Name the blood parasite species.
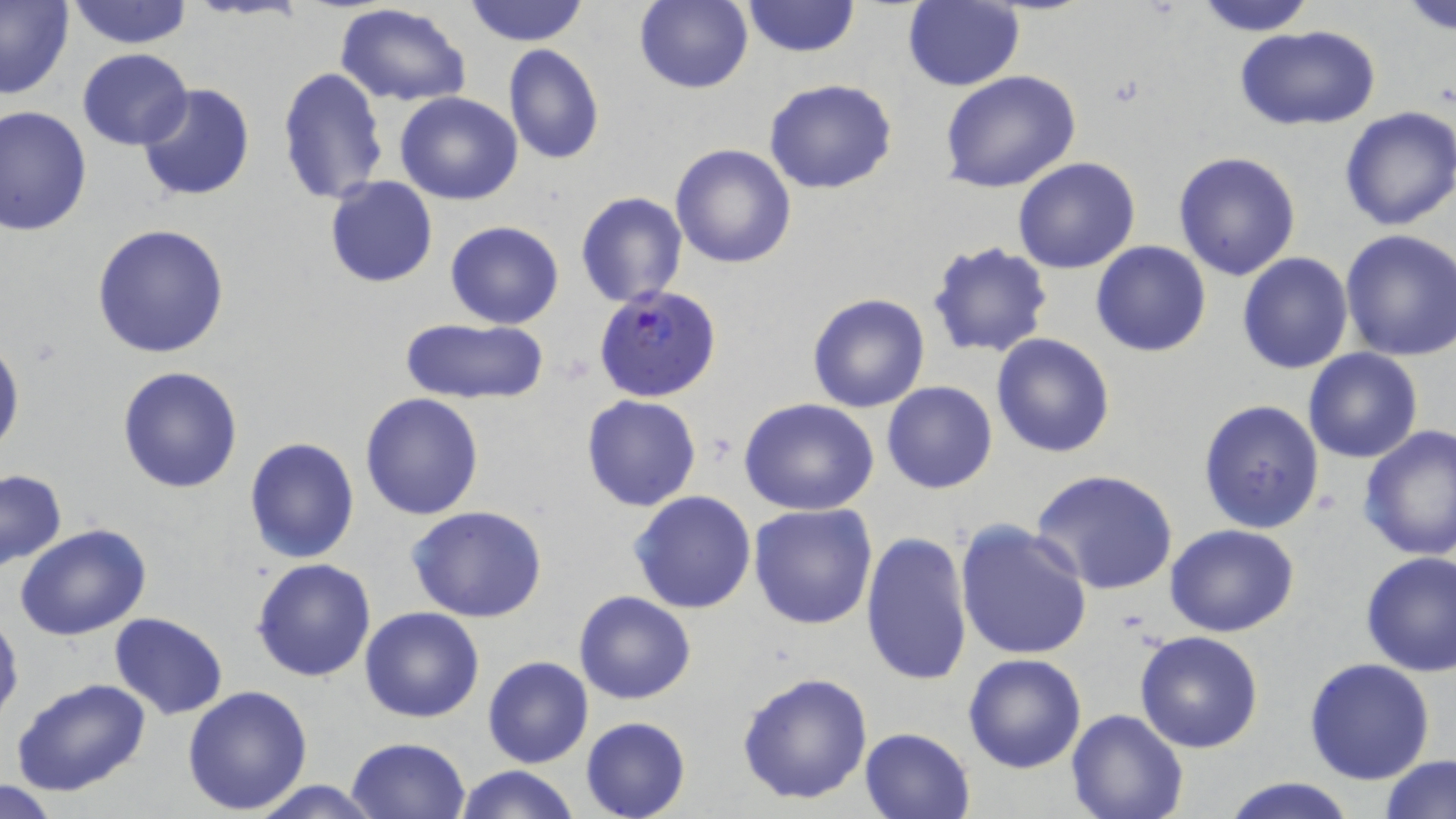

Plasmodium falciparum.

Summary:
  - Coordinate format: approximate bounding boxes as (x1, y1, x2, y2) in pixels
  - Uninfected red blood cell locations: (0, 0, 78, 101), (463, 0, 590, 46), (631, 0, 754, 95), (1190, 0, 1319, 35), (65, 1, 194, 50), (741, 1, 860, 58), (1397, 1, 1456, 35), (901, 2, 1025, 90), (334, 4, 474, 107), (1234, 25, 1382, 130), (502, 45, 604, 165), (77, 49, 192, 150), (277, 66, 390, 207), (937, 69, 1081, 194), (763, 79, 898, 195), (135, 83, 254, 202), (396, 91, 523, 205), (0, 103, 94, 236), (1338, 105, 1456, 232), (670, 144, 797, 268), (1172, 151, 1302, 282), (1013, 157, 1141, 274), (324, 175, 438, 288), (575, 192, 688, 307), (445, 221, 564, 329), (92, 223, 230, 360), (1338, 229, 1456, 361), (926, 240, 1055, 358), (1090, 240, 1212, 358), (1236, 252, 1355, 374), (806, 292, 931, 413), (398, 316, 549, 405), (990, 332, 1116, 458), (0, 334, 24, 461), (1302, 348, 1423, 462), (115, 365, 243, 494), (881, 380, 997, 494), (360, 392, 486, 520), (580, 393, 703, 511), (739, 399, 880, 515), (1198, 399, 1326, 536), (1357, 424, 1456, 564), (244, 436, 360, 565), (1030, 468, 1178, 595), (1, 470, 67, 571), (628, 489, 758, 613), (748, 503, 879, 630), (407, 505, 550, 623), (952, 520, 1094, 662), (1164, 524, 1299, 637), (14, 526, 151, 642), (860, 529, 974, 687), (1358, 552, 1456, 678), (251, 556, 378, 682), (574, 590, 696, 706), (0, 606, 23, 730), (359, 606, 485, 723), (109, 612, 228, 719), (1133, 631, 1264, 754), (963, 653, 1087, 774), (482, 655, 593, 768), (1303, 658, 1435, 785), (736, 671, 873, 806), (11, 678, 154, 799), (181, 685, 314, 814), (1064, 710, 1188, 819), (580, 717, 691, 819), (858, 726, 976, 819), (346, 737, 473, 819), (1378, 753, 1456, 818), (453, 764, 581, 819), (1220, 776, 1360, 819), (246, 778, 384, 817), (1, 781, 63, 817)
  - Plasmodium falciparum-infected red blood cell locations: (594, 284, 723, 403)
  - Image size: 1456×819 pixels
  - Magnification: 1000x
  - Stain: May-Grünwald-Giemsa
  - Modality: light microscopy
  - Preparation: thin blood smear
  - Field of view: single